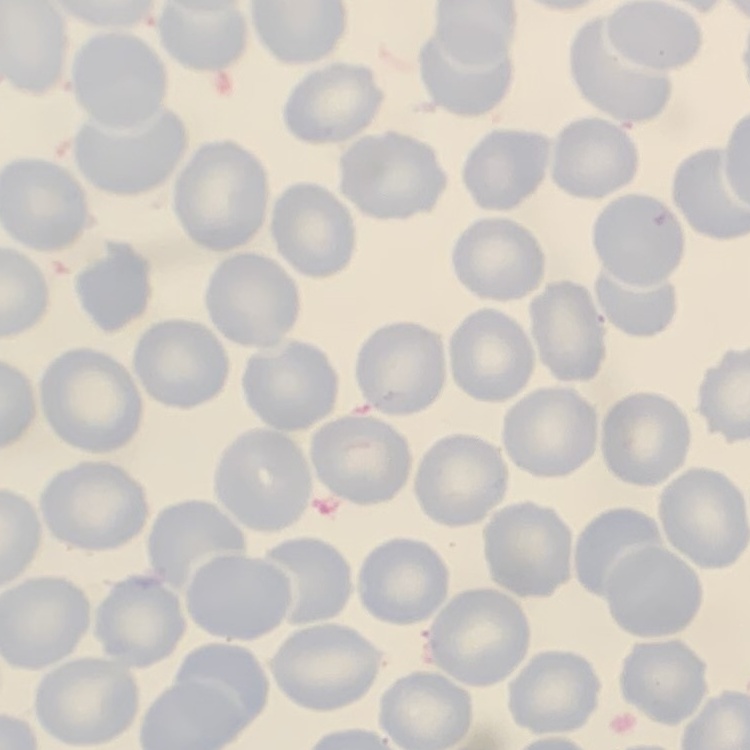

Summary:
  - Erythrocyte morphology: no rouleaux formation
  - Stain: Field's or Giemsa
  - Preparation: thin blood smear
  - Image type: one tile cut from a larger photomicrograph